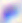

magnification = 400x
modality = photomicrograph
identification = Toxoplasma gondii